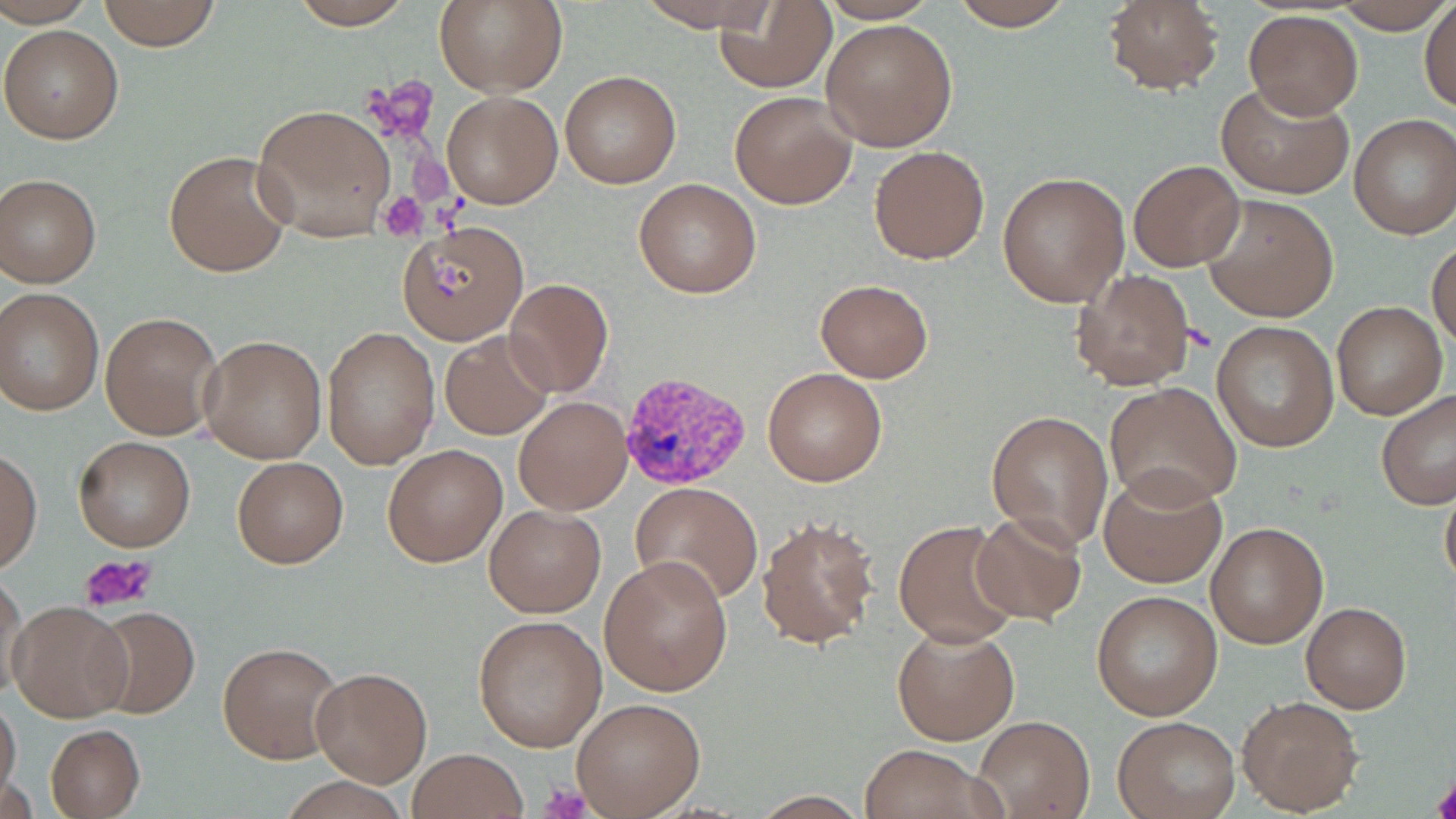 Approximate bounding boxes as (x1,y1)-(x2,y2) corner pairs in pixels. Uninfected red blood cell locations: (0,0)-(94,26), (96,0)-(221,50), (433,0)-(567,96), (816,0)-(938,24), (947,0)-(1080,29), (1100,0)-(1225,95), (1333,0)-(1454,35), (283,1)-(421,29), (633,1)-(783,32), (1419,1)-(1455,113), (715,4)-(835,92), (1244,10)-(1363,118), (821,18)-(957,152), (2,24)-(125,145), (560,70)-(681,189), (1215,81)-(1354,200), (441,90)-(562,209), (729,91)-(857,209), (252,103)-(396,241), (1350,114)-(1456,239), (869,144)-(989,264), (164,149)-(292,279), (1129,159)-(1246,273), (997,170)-(1130,307), (0,174)-(101,287), (632,178)-(763,299), (1201,192)-(1339,322), (397,221)-(529,343), (1428,241)-(1456,350), (1070,268)-(1196,391), (504,277)-(614,397), (815,279)-(932,382), (0,288)-(104,415), (1331,300)-(1447,420), (101,311)-(223,439), (1211,320)-(1338,452), (321,326)-(439,471), (440,332)-(555,440), (201,334)-(326,464), (761,368)-(887,486), (1105,382)-(1242,509), (1377,389)-(1456,512), (514,395)-(631,513), (986,410)-(1114,548), (72,436)-(196,552), (383,444)-(507,566), (0,446)-(42,576), (231,456)-(348,568), (1098,465)-(1227,589), (1439,477)-(1456,595), (631,480)-(763,605), (484,503)-(605,617), (968,512)-(1088,626), (755,513)-(881,652), (893,520)-(1022,648), (1205,521)-(1329,649), (600,554)-(732,695), (1,570)-(28,702), (1091,590)-(1223,721), (1299,601)-(1412,713), (8,602)-(133,721), (85,605)-(202,719), (473,614)-(607,751), (891,622)-(1019,746), (218,639)-(342,765), (310,667)-(433,788), (1238,695)-(1364,815), (571,697)-(705,817), (0,698)-(22,806), (1112,714)-(1240,819), (976,715)-(1093,818), (45,723)-(144,817), (858,744)-(997,819), (407,748)-(527,818). Platelet locations: (378,191)-(428,238), (80,553)-(159,615), (1431,777)-(1456,818), (540,783)-(591,818). Plasmodium vivax-infected red blood cell locations: (617,369)-(755,493). Slide-level diagnosis: Plasmodium vivax. 1000x magnification. Thin blood film. Single field of view. Image is 1456×819 pixels. May-Grünwald-Giemsa-stained preparation. Optical microscopy.